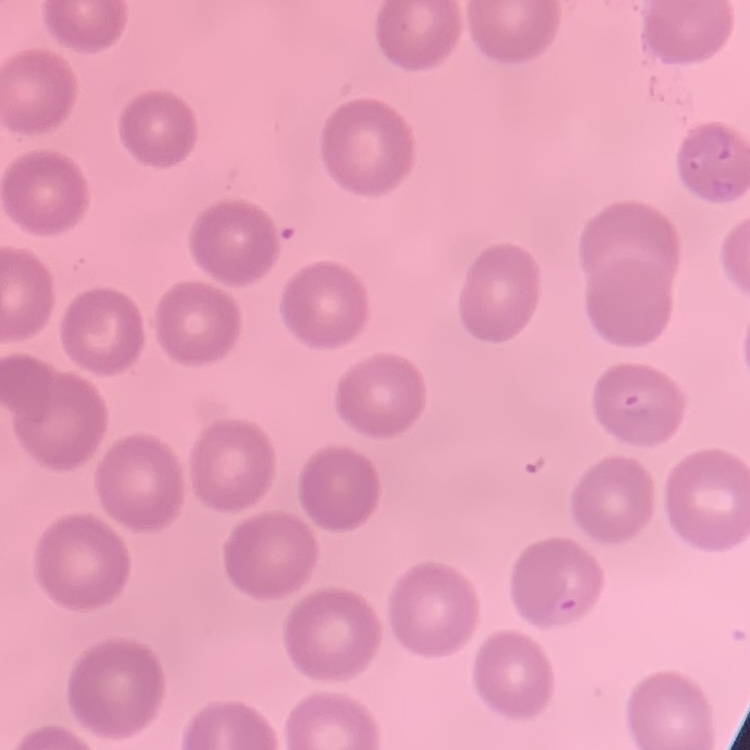
erythrocyte morphology = no rouleaux formation
stain = Field's or Giemsa
preparation = thin peripheral smear
image type = square crop of a larger photomicrograph